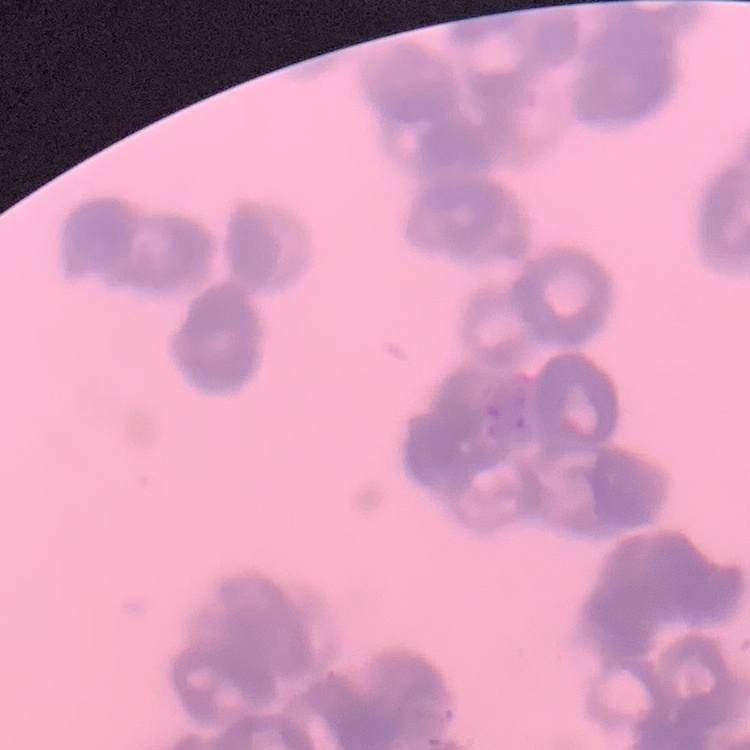 The red blood cells exhibit rouleaux formation. Field's or Giemsa stain. Square crop of a larger photomicrograph. Thin peripheral smear.